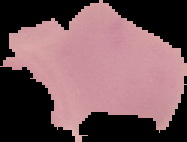
Malaria status: uninfected. From a thin blood film. Segmented cell region on a black background. Image is 187×142 pixels.